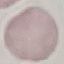

Summary:
  - Result: no malaria parasites seen
  - Capture: smartphone through the microscope eyepiece
  - Image type: cell patch, automatically extracted from a larger field of view and resized to 64 × 64 pixels
  - Preparation: thin smear
  - Stain: Giemsa